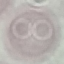
Summary:
  - Result: no malaria parasites seen
  - Image type: automatically extracted cell patch, resized to 64 × 64 pixels
  - Capture: smartphone through the microscope eyepiece
  - Stain: Giemsa
  - Preparation: thin blood film